Outline each blood parasite and name the species.
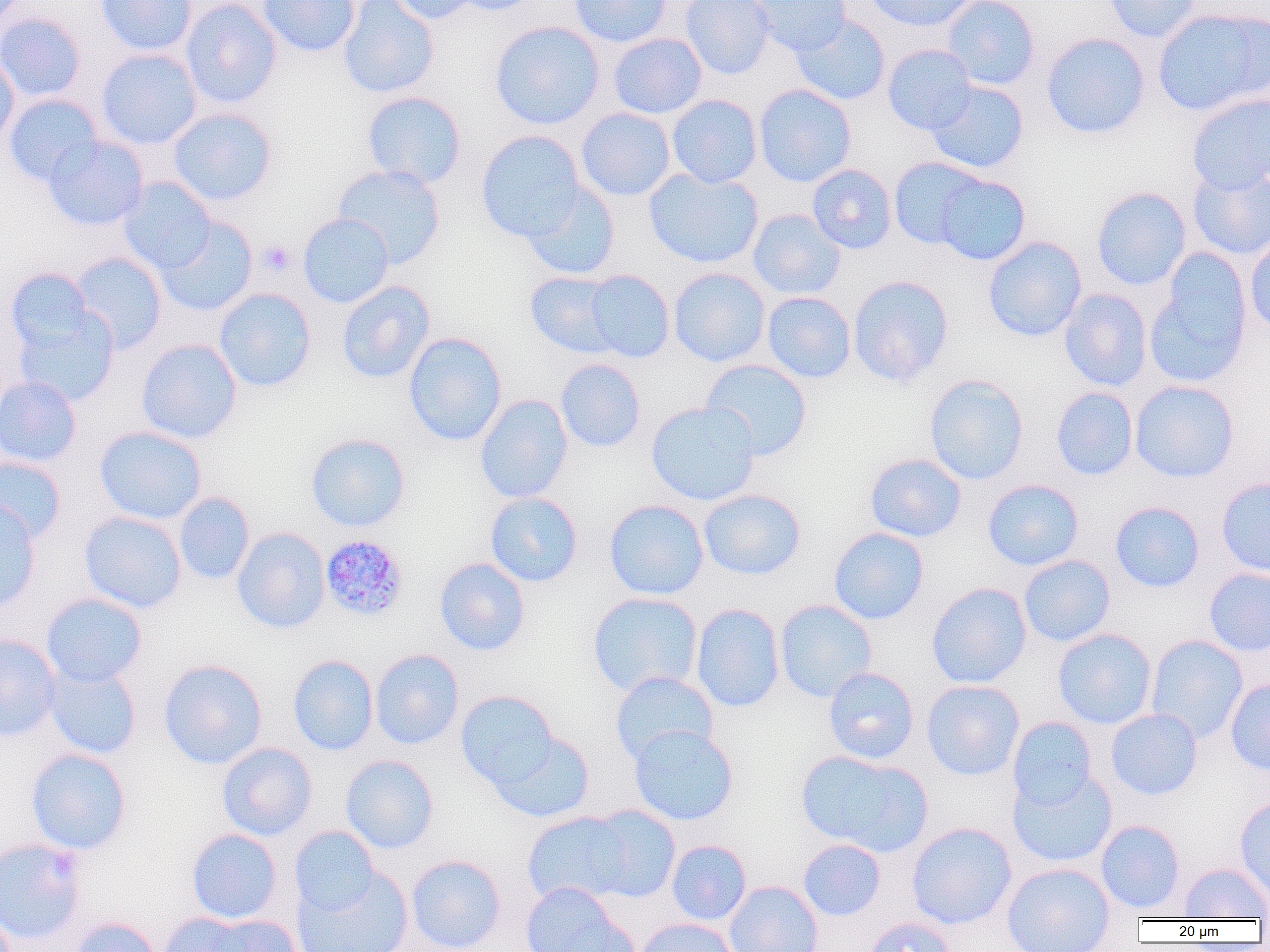

Approximate bounding boxes as named x1/y1/x2/y2 corners in pixels.
Plasmodium malariae-infected red blood cells: (x1=320, y1=534, x2=408, y2=621).
No Plasmodium falciparum, Plasmodium ovale, Plasmodium vivax, Babesia divergens, or Trypanosoma brucei observed.

Summary:
  - Platelet locations: (x1=258, y1=240, x2=295, y2=276)
  - Uninfected red blood cell locations: (x1=95, y1=0, x2=198, y2=56), (x1=180, y1=0, x2=281, y2=109), (x1=257, y1=0, x2=361, y2=57), (x1=337, y1=0, x2=439, y2=98), (x1=387, y1=0, x2=481, y2=24), (x1=448, y1=0, x2=545, y2=16), (x1=569, y1=0, x2=673, y2=47), (x1=680, y1=0, x2=775, y2=79), (x1=749, y1=0, x2=850, y2=56), (x1=863, y1=0, x2=977, y2=32), (x1=941, y1=0, x2=1040, y2=90), (x1=1102, y1=0, x2=1202, y2=43), (x1=1152, y1=7, x2=1270, y2=116), (x1=0, y1=12, x2=86, y2=102), (x1=791, y1=14, x2=891, y2=106), (x1=490, y1=21, x2=604, y2=130), (x1=1041, y1=32, x2=1150, y2=139), (x1=608, y1=33, x2=707, y2=119), (x1=882, y1=43, x2=977, y2=136), (x1=96, y1=48, x2=202, y2=149), (x1=0, y1=51, x2=19, y2=150), (x1=927, y1=80, x2=1029, y2=174), (x1=754, y1=84, x2=857, y2=187), (x1=360, y1=91, x2=467, y2=189), (x1=1187, y1=93, x2=1270, y2=193), (x1=4, y1=94, x2=104, y2=186), (x1=667, y1=94, x2=762, y2=188), (x1=576, y1=107, x2=676, y2=201), (x1=168, y1=108, x2=277, y2=206), (x1=476, y1=130, x2=586, y2=242), (x1=43, y1=136, x2=148, y2=230), (x1=889, y1=157, x2=988, y2=250), (x1=332, y1=164, x2=445, y2=269), (x1=807, y1=164, x2=897, y2=254), (x1=1187, y1=164, x2=1270, y2=261), (x1=644, y1=167, x2=763, y2=268), (x1=933, y1=173, x2=1031, y2=265), (x1=118, y1=177, x2=216, y2=274), (x1=521, y1=181, x2=620, y2=280), (x1=1091, y1=186, x2=1191, y2=291), (x1=747, y1=209, x2=846, y2=300), (x1=298, y1=213, x2=394, y2=308), (x1=155, y1=216, x2=257, y2=317), (x1=1245, y1=233, x2=1270, y2=338), (x1=983, y1=236, x2=1087, y2=341), (x1=1145, y1=250, x2=1254, y2=389), (x1=70, y1=251, x2=167, y2=354), (x1=5, y1=268, x2=97, y2=357), (x1=668, y1=268, x2=770, y2=367), (x1=581, y1=270, x2=674, y2=363), (x1=525, y1=271, x2=625, y2=358), (x1=847, y1=275, x2=953, y2=388), (x1=337, y1=281, x2=435, y2=384), (x1=213, y1=288, x2=316, y2=392), (x1=1059, y1=288, x2=1152, y2=392), (x1=762, y1=291, x2=856, y2=383), (x1=12, y1=304, x2=119, y2=407), (x1=403, y1=332, x2=507, y2=446), (x1=136, y1=338, x2=242, y2=444), (x1=555, y1=359, x2=646, y2=453), (x1=700, y1=359, x2=812, y2=461), (x1=925, y1=374, x2=1028, y2=485), (x1=0, y1=375, x2=81, y2=467), (x1=1130, y1=380, x2=1239, y2=483), (x1=1051, y1=387, x2=1138, y2=480), (x1=474, y1=394, x2=573, y2=503), (x1=645, y1=401, x2=760, y2=506), (x1=94, y1=426, x2=207, y2=525), (x1=305, y1=432, x2=410, y2=532), (x1=865, y1=453, x2=966, y2=543), (x1=0, y1=456, x2=66, y2=544), (x1=1216, y1=477, x2=1270, y2=577), (x1=983, y1=478, x2=1084, y2=571), (x1=699, y1=488, x2=806, y2=580), (x1=174, y1=492, x2=255, y2=584), (x1=484, y1=492, x2=583, y2=587), (x1=0, y1=499, x2=41, y2=614), (x1=604, y1=499, x2=709, y2=600), (x1=1109, y1=501, x2=1205, y2=593), (x1=79, y1=511, x2=187, y2=613), (x1=232, y1=527, x2=330, y2=633), (x1=829, y1=527, x2=929, y2=625), (x1=1019, y1=555, x2=1115, y2=647), (x1=434, y1=557, x2=530, y2=656), (x1=1203, y1=568, x2=1270, y2=656), (x1=926, y1=582, x2=1032, y2=688), (x1=587, y1=591, x2=703, y2=698), (x1=41, y1=593, x2=147, y2=686), (x1=775, y1=599, x2=877, y2=702), (x1=691, y1=603, x2=785, y2=712), (x1=1053, y1=628, x2=1157, y2=729), (x1=0, y1=633, x2=61, y2=741), (x1=1145, y1=634, x2=1248, y2=743), (x1=370, y1=649, x2=464, y2=750), (x1=288, y1=654, x2=379, y2=755), (x1=158, y1=658, x2=267, y2=769), (x1=44, y1=661, x2=142, y2=760), (x1=823, y1=667, x2=919, y2=764), (x1=610, y1=671, x2=718, y2=765), (x1=1225, y1=679, x2=1270, y2=776), (x1=921, y1=680, x2=1024, y2=780), (x1=455, y1=690, x2=561, y2=794), (x1=1105, y1=708, x2=1203, y2=800), (x1=1007, y1=716, x2=1098, y2=811), (x1=628, y1=724, x2=739, y2=825), (x1=489, y1=728, x2=595, y2=823), (x1=217, y1=742, x2=317, y2=840), (x1=26, y1=748, x2=131, y2=854), (x1=797, y1=751, x2=930, y2=856), (x1=340, y1=755, x2=439, y2=854), (x1=1007, y1=768, x2=1117, y2=868), (x1=1234, y1=795, x2=1270, y2=903), (x1=581, y1=805, x2=681, y2=902), (x1=521, y1=810, x2=637, y2=907), (x1=1095, y1=820, x2=1185, y2=914), (x1=907, y1=822, x2=1017, y2=929), (x1=289, y1=826, x2=380, y2=916), (x1=186, y1=828, x2=283, y2=923), (x1=0, y1=837, x2=87, y2=946), (x1=798, y1=839, x2=886, y2=920), (x1=666, y1=840, x2=751, y2=926), (x1=406, y1=854, x2=506, y2=952), (x1=1002, y1=862, x2=1115, y2=952), (x1=1179, y1=862, x2=1270, y2=920), (x1=292, y1=864, x2=414, y2=952), (x1=724, y1=881, x2=823, y2=952), (x1=519, y1=882, x2=631, y2=952), (x1=157, y1=912, x2=266, y2=952), (x1=198, y1=915, x2=302, y2=952), (x1=68, y1=916, x2=162, y2=952), (x1=860, y1=916, x2=957, y2=952), (x1=635, y1=918, x2=740, y2=952)
  - Slide-level diagnosis: Plasmodium malariae
  - Image size: 1270×952 pixels
  - Magnification: 1000x
  - Preparation: thin blood film
  - Field of view: one of a larger specimen
  - Modality: light microscopy